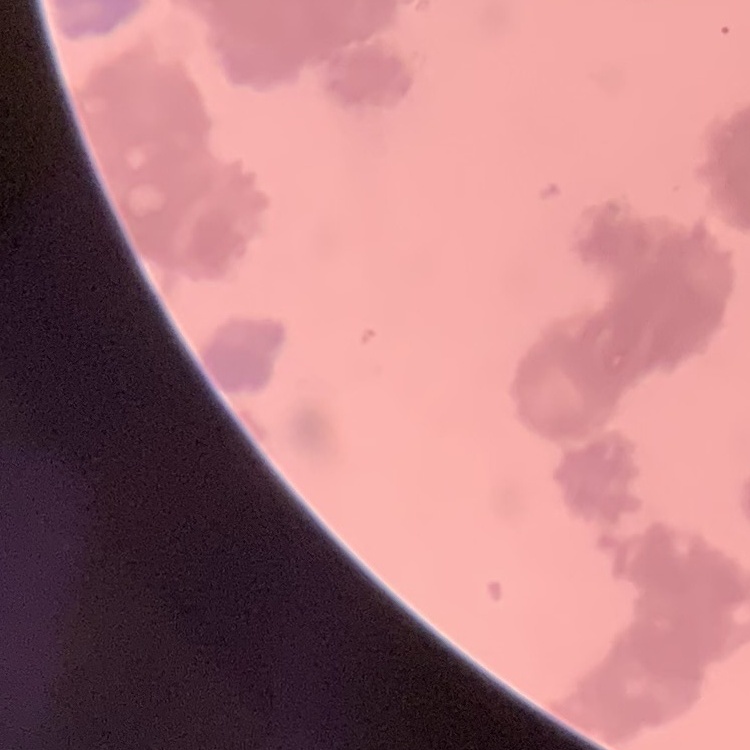 The erythrocytes show rouleaux formation. Thin blood film. Field's or Giemsa stain. Square crop of a larger photomicrograph.